Name the blood parasite species.
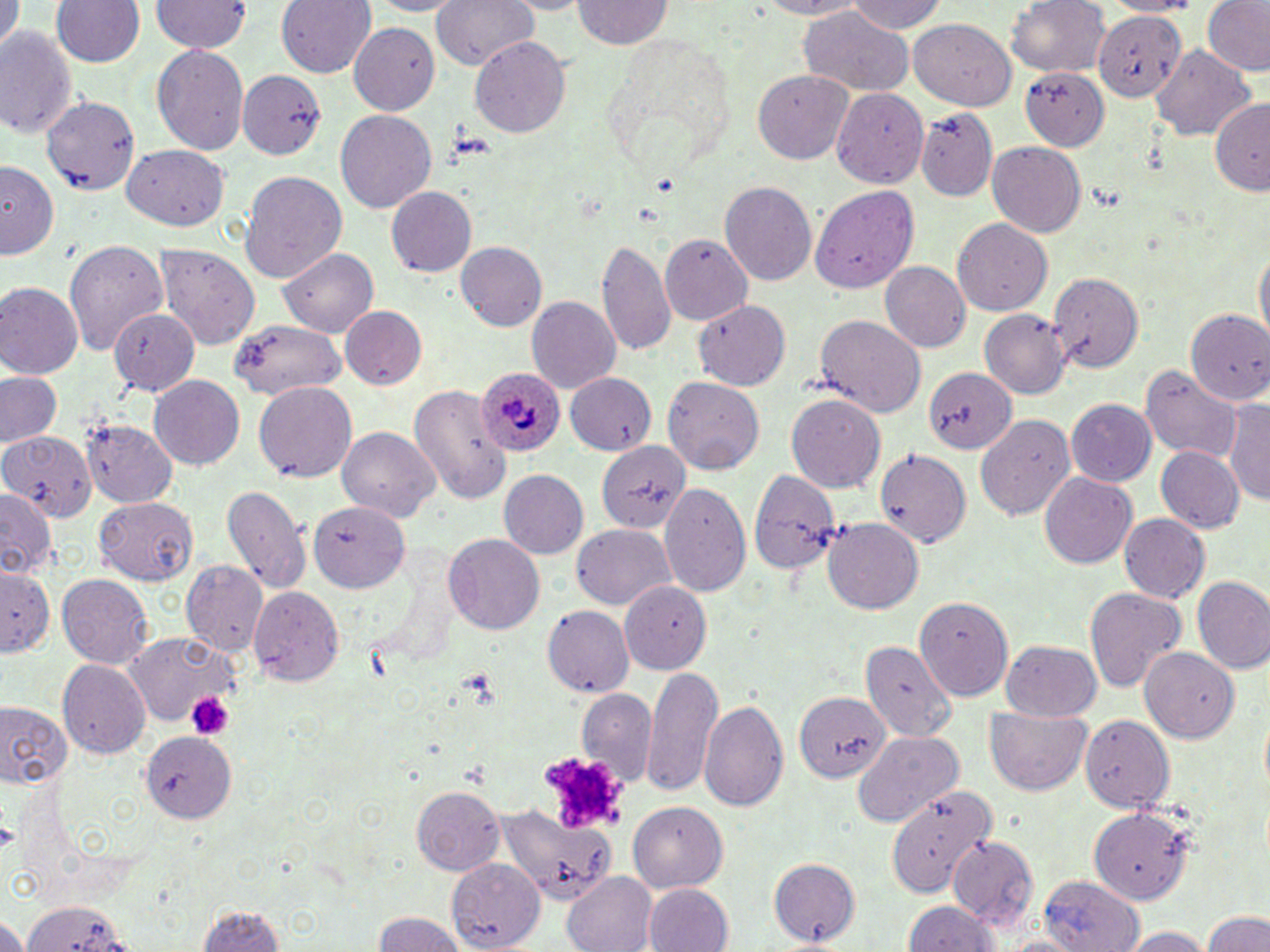

Plasmodium ovale.

preparation: thin blood smear
plasmodium_ovale_infected_red_blood_cell_locations: 'approximate bounding boxes as (x1,y1)-(x2,y2) corner pairs in pixels: (475,363)-(569,458)'
magnification: 1000x
stain: May-Grünwald-Giemsa
modality: optical microscopy
image_size: 1270×952 pixels
field_of_view: one of a larger specimen
platelet_locations: 'approximate bounding boxes as (x1,y1)-(x2,y2) corner pairs in pixels: (460,669)-(503,708), (187,691)-(232,740), (539,750)-(625,829)'
uninfected_red_blood_cell_locations: 'approximate bounding boxes as (x1,y1)-(x2,y2) corner pairs in pixels: (49,0)-(146,69), (151,0)-(250,55), (278,0)-(374,78), (434,0)-(539,74), (751,0)-(878,19), (845,0)-(949,34), (1005,0)-(1111,80), (1097,0)-(1202,17), (1201,0)-(1269,76), (575,1)-(671,51), (3,2)-(22,48), (797,6)-(911,98), (1094,11)-(1184,103), (911,18)-(1018,109), (350,21)-(441,113), (0,27)-(80,141), (606,28)-(737,166), (469,36)-(571,140), (1150,41)-(1254,140), (155,43)-(249,158), (1021,67)-(1109,150), (241,69)-(325,160), (753,69)-(854,164), (832,89)-(929,187), (42,94)-(141,197), (1206,94)-(1270,194), (335,109)-(437,212), (918,109)-(999,200), (987,140)-(1086,235), (124,146)-(229,231), (2,162)-(60,263), (240,171)-(347,283), (720,180)-(818,289), (388,186)-(477,277), (809,187)-(919,293), (953,221)-(1052,314), (661,234)-(752,323), (599,237)-(675,356), (64,238)-(169,354), (454,240)-(546,332), (155,243)-(261,347), (1253,245)-(1269,349), (279,247)-(379,337), (881,262)-(971,354), (1047,268)-(1145,373), (0,282)-(81,380), (527,298)-(621,393), (694,299)-(790,389), (1186,304)-(1270,405), (340,306)-(429,389), (110,308)-(200,397), (980,310)-(1071,401), (815,314)-(926,417), (233,318)-(344,399), (917,364)-(1013,457), (1139,364)-(1243,463), (1,371)-(64,450), (565,373)-(658,455), (149,376)-(245,472), (664,376)-(763,475), (407,381)-(508,506), (254,382)-(357,482), (787,395)-(885,492), (1226,399)-(1270,507), (1065,400)-(1158,486), (976,414)-(1074,520), (83,421)-(177,508), (338,426)-(438,523), (0,430)-(97,520), (596,439)-(690,535), (1154,445)-(1244,533), (875,448)-(971,549), (746,466)-(839,579), (499,470)-(589,560), (1039,472)-(1136,570), (659,482)-(751,597), (221,484)-(310,593), (0,489)-(57,581), (96,496)-(199,583), (303,499)-(411,595), (1120,514)-(1210,603), (822,518)-(924,614), (572,524)-(676,611), (442,533)-(544,635), (183,563)-(269,656), (1,565)-(56,660), (57,573)-(152,666), (1192,578)-(1270,675), (621,582)-(711,673), (249,583)-(344,685), (1083,585)-(1188,693), (914,596)-(1015,698), (543,608)-(634,696), (125,630)-(241,727), (1000,640)-(1103,721), (863,645)-(956,740), (1141,646)-(1242,743), (58,660)-(150,759), (645,665)-(721,797), (578,689)-(656,788), (787,691)-(886,784), (700,698)-(789,815), (0,702)-(71,791), (985,709)-(1094,796), (1079,714)-(1174,811), (140,729)-(235,821), (853,731)-(963,828), (411,787)-(504,874), (884,789)-(992,895), (629,800)-(725,891), (1091,800)-(1198,905), (498,803)-(613,901), (949,837)-(1037,930), (769,858)-(860,947), (449,861)-(545,950), (563,873)-(657,952), (1037,874)-(1143,952), (645,884)-(734,952), (21,898)-(129,952), (904,899)-(1003,952), (194,903)-(289,952), (1201,908)-(1269,952), (370,911)-(472,952), (0,916)-(25,952), (1118,927)-(1214,952)'